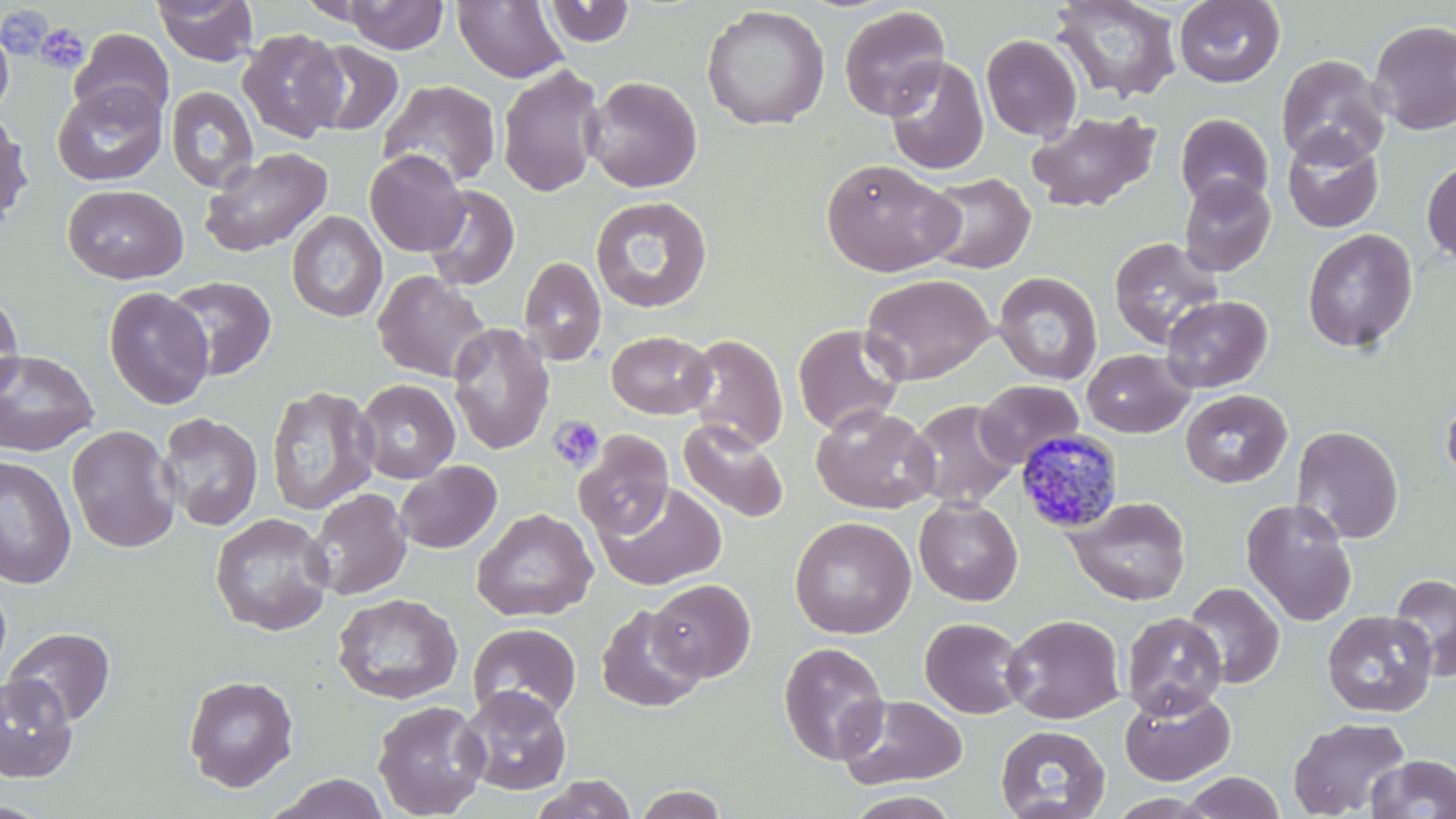

Summary:
  - Coordinate format: approximate bounding boxes as (x1, y1, x2, y2) in pixels
  - Uninfected red blood cell locations: (153, 0, 258, 66), (340, 0, 449, 54), (452, 0, 569, 84), (1051, 0, 1182, 104), (1173, 0, 1285, 88), (544, 1, 636, 47), (701, 5, 830, 131), (839, 5, 950, 120), (1369, 19, 1456, 135), (0, 22, 14, 118), (69, 28, 174, 123), (237, 28, 348, 143), (981, 34, 1083, 141), (304, 41, 404, 137), (1276, 54, 1390, 168), (884, 56, 988, 175), (496, 64, 606, 197), (584, 75, 703, 193), (378, 80, 501, 188), (52, 83, 167, 186), (165, 85, 259, 192), (1026, 109, 1161, 213), (0, 110, 34, 230), (1175, 113, 1273, 209), (1282, 130, 1384, 233), (1291, 130, 1402, 337), (199, 146, 332, 258), (365, 150, 469, 256), (821, 158, 962, 277), (1422, 159, 1456, 267), (922, 172, 1035, 274), (1179, 174, 1276, 276), (62, 184, 188, 284), (421, 185, 520, 291), (590, 196, 713, 314), (286, 211, 387, 322), (1302, 228, 1418, 354), (1108, 236, 1225, 349), (518, 256, 606, 366), (372, 270, 490, 382), (993, 272, 1103, 385), (861, 273, 996, 385), (163, 276, 277, 381), (103, 287, 214, 410), (0, 291, 24, 400), (1161, 295, 1272, 393), (447, 323, 554, 455), (793, 323, 906, 436), (606, 330, 716, 419), (683, 334, 788, 451), (0, 349, 99, 457), (1082, 349, 1195, 438), (355, 379, 460, 484), (975, 379, 1084, 468), (265, 385, 380, 515), (1440, 386, 1456, 491), (1180, 389, 1292, 488), (907, 400, 1020, 509), (811, 404, 939, 514), (159, 405, 380, 523), (156, 412, 263, 531), (678, 418, 789, 524), (65, 424, 181, 553), (1291, 425, 1404, 543), (574, 430, 674, 539), (0, 454, 77, 590), (395, 461, 502, 554), (595, 482, 727, 591), (306, 487, 412, 601), (1066, 496, 1191, 606), (914, 497, 1023, 606), (1240, 497, 1358, 626), (472, 507, 598, 622), (209, 513, 335, 636), (789, 516, 916, 639), (1389, 573, 1456, 680), (648, 578, 756, 682), (1183, 581, 1285, 689), (332, 592, 462, 705), (596, 604, 705, 713), (1322, 609, 1437, 717), (1121, 612, 1227, 719), (1002, 614, 1125, 724), (919, 617, 1028, 719), (467, 623, 582, 722), (4, 627, 116, 727), (778, 642, 890, 765), (0, 673, 78, 782), (183, 674, 299, 792), (458, 685, 572, 795), (1120, 688, 1235, 786), (837, 694, 969, 790), (372, 699, 489, 818), (1288, 716, 1411, 818), (995, 724, 1110, 819), (1365, 753, 1456, 818), (1182, 772, 1285, 819), (268, 773, 391, 818), (530, 774, 637, 819), (632, 785, 730, 819), (844, 790, 962, 818), (0, 799, 54, 818)
  - Platelet locations: (35, 23, 90, 74), (549, 416, 605, 472)
  - Plasmodium malariae-infected red blood cell locations: (1016, 428, 1125, 533)
  - Slide-level diagnosis: Plasmodium malariae
  - Magnification: 1000x
  - Modality: light microscopy
  - Stain: May-Grünwald-Giemsa
  - Field of view: single
  - Image size: 1456×819 pixels
  - Preparation: thin blood smear